Name the cell type shown.
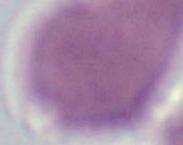

An erythrocyte.

modality: photomicrograph
magnification: 1000x